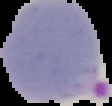

Summary:
  - Result: Plasmodium parasites detected
  - Image size: 112×106 pixels
  - Preparation: thin blood smear
  - Image type: segmented cell region on a black background